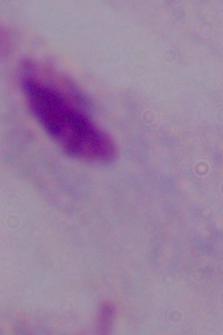

identification = trichomonad
modality = photomicrograph
magnification = 1000x